Assess this cell for malaria.
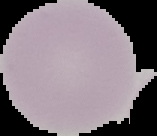

Uninfected.

From a thin blood film. Cell region segmented out of the field of view; the surrounding area is masked to black. Image is 157×136 pixels.